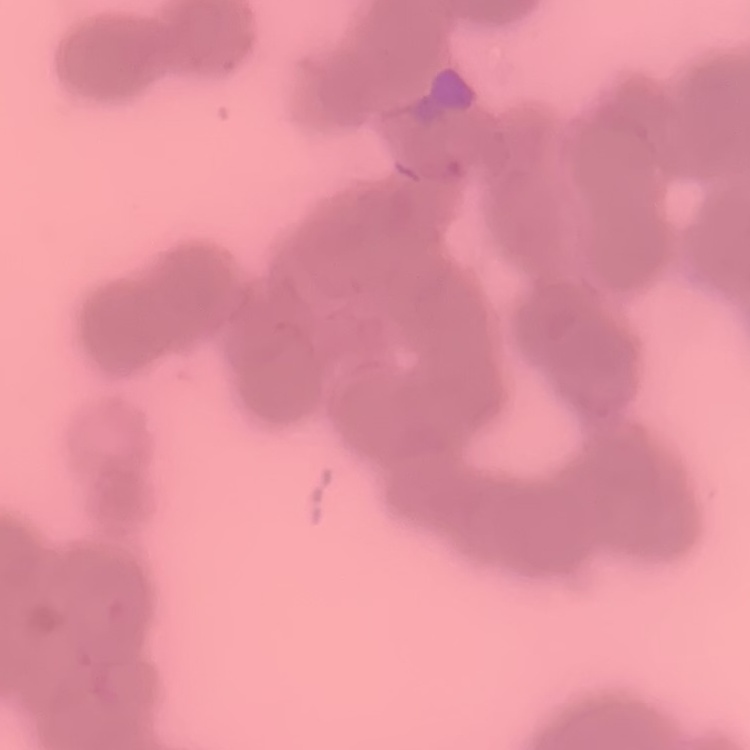

erythrocyte_morphology: rouleaux formation
stain: Field's or Giemsa
preparation: thin blood film
image_type: square crop of a larger photomicrograph